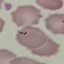

result = no malaria parasites seen
image type = cell patch, automatically extracted from a larger field of view and resized to 64 × 64 pixels
preparation = thin blood film
capture = smartphone camera at the microscope eyepiece
stain = Giemsa